Locate and identify every blood parasite.
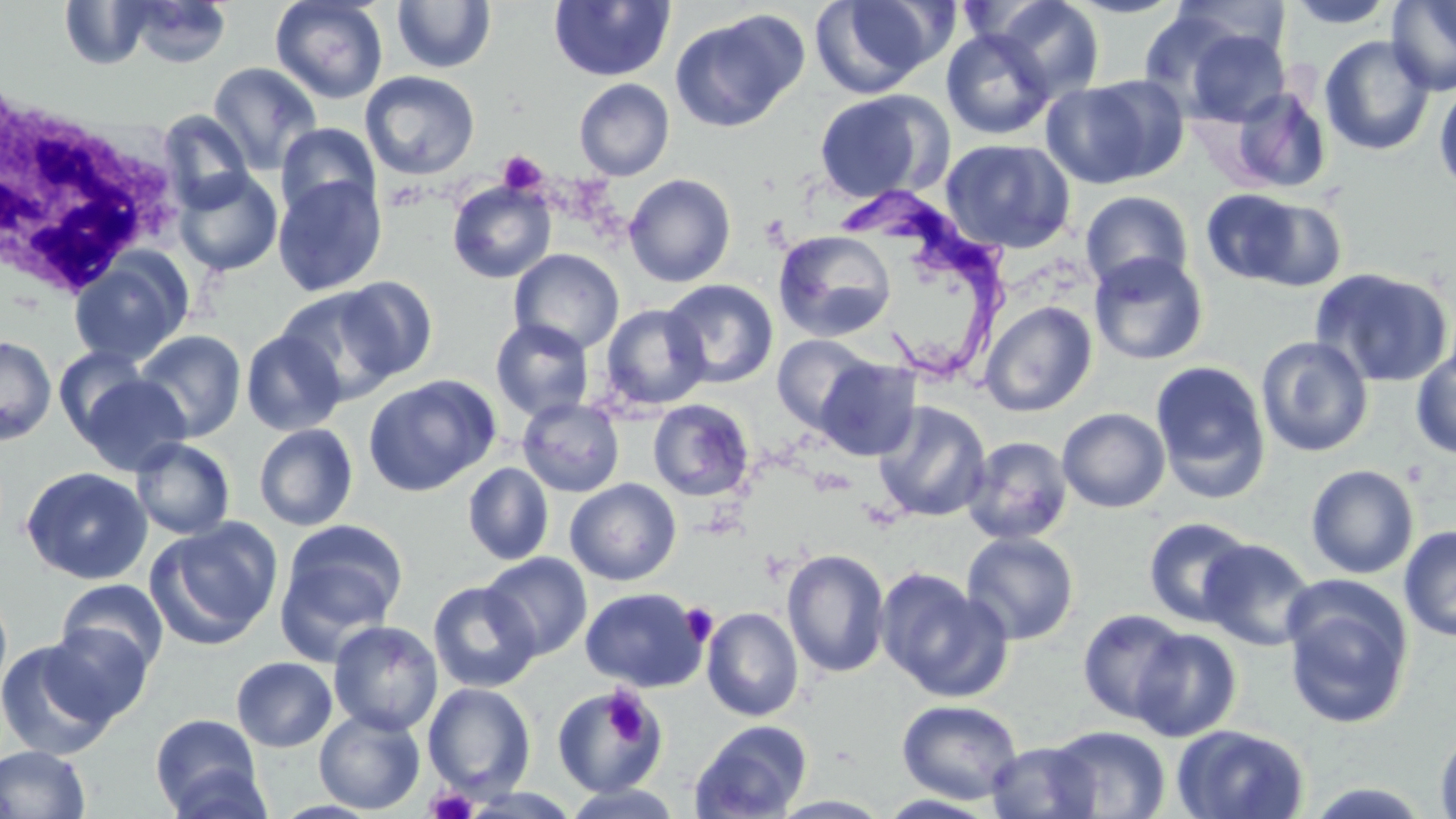

Approximate bounding boxes as named x1/y1/x2/y2 corners in pixels.
Trypanosoma brucei: (x1=843, y1=188, x2=1015, y2=387).
No Plasmodium falciparum, Plasmodium ovale, Plasmodium malariae, Plasmodium vivax, or Babesia divergens observed.

slide-level diagnosis = Trypanosoma brucei
field of view = single
stain = May-Grünwald-Giemsa
white blood cell locations = approximate bounding boxes as named x1/y1/x2/y2 corners in pixels: (x1=1, y1=98, x2=186, y2=296)
modality = light microscopy
platelet locations = approximate bounding boxes as named x1/y1/x2/y2 corners in pixels: (x1=497, y1=150, x2=547, y2=196), (x1=678, y1=602, x2=719, y2=646), (x1=601, y1=689, x2=660, y2=747), (x1=425, y1=786, x2=479, y2=819)
image size = 1456×819 pixels
magnification = 1000x
preparation = thin blood film
uninfected red blood cell locations = approximate bounding boxes as named x1/y1/x2/y2 corners in pixels: (x1=270, y1=0, x2=389, y2=104), (x1=391, y1=0, x2=496, y2=74), (x1=810, y1=0, x2=946, y2=98), (x1=988, y1=0, x2=1105, y2=102), (x1=1065, y1=0, x2=1187, y2=19), (x1=1167, y1=0, x2=1292, y2=66), (x1=1284, y1=0, x2=1399, y2=28), (x1=1387, y1=0, x2=1456, y2=96), (x1=59, y1=1, x2=152, y2=69), (x1=548, y1=1, x2=675, y2=82), (x1=124, y1=2, x2=233, y2=68), (x1=1138, y1=7, x2=1255, y2=114), (x1=670, y1=10, x2=809, y2=133), (x1=941, y1=29, x2=1055, y2=140), (x1=1182, y1=29, x2=1291, y2=127), (x1=1319, y1=35, x2=1435, y2=156), (x1=207, y1=61, x2=323, y2=175), (x1=359, y1=71, x2=480, y2=180), (x1=1042, y1=77, x2=1176, y2=188), (x1=574, y1=78, x2=674, y2=181), (x1=1434, y1=80, x2=1456, y2=197), (x1=1229, y1=86, x2=1332, y2=194), (x1=812, y1=90, x2=948, y2=204), (x1=156, y1=110, x2=254, y2=212), (x1=275, y1=123, x2=380, y2=222), (x1=940, y1=138, x2=1076, y2=254), (x1=173, y1=168, x2=283, y2=276), (x1=624, y1=173, x2=736, y2=287), (x1=272, y1=175, x2=387, y2=296), (x1=447, y1=181, x2=556, y2=284), (x1=1201, y1=188, x2=1309, y2=286), (x1=1080, y1=190, x2=1194, y2=293), (x1=1240, y1=195, x2=1350, y2=293), (x1=773, y1=230, x2=898, y2=342), (x1=509, y1=249, x2=624, y2=355), (x1=68, y1=251, x2=193, y2=367), (x1=1088, y1=252, x2=1209, y2=366), (x1=1310, y1=267, x2=1454, y2=388), (x1=335, y1=276, x2=439, y2=382), (x1=662, y1=279, x2=778, y2=388), (x1=275, y1=286, x2=402, y2=404), (x1=979, y1=301, x2=1097, y2=417), (x1=599, y1=303, x2=712, y2=411), (x1=490, y1=318, x2=595, y2=422), (x1=240, y1=329, x2=347, y2=436), (x1=134, y1=330, x2=246, y2=441), (x1=771, y1=334, x2=878, y2=433), (x1=1256, y1=335, x2=1374, y2=457), (x1=0, y1=336, x2=56, y2=445), (x1=56, y1=346, x2=152, y2=444), (x1=1411, y1=351, x2=1456, y2=459), (x1=814, y1=358, x2=921, y2=461), (x1=1150, y1=360, x2=1271, y2=503), (x1=78, y1=374, x2=191, y2=475), (x1=363, y1=375, x2=500, y2=497), (x1=517, y1=398, x2=625, y2=497), (x1=647, y1=399, x2=754, y2=501), (x1=874, y1=401, x2=990, y2=521), (x1=1057, y1=408, x2=1170, y2=513), (x1=253, y1=423, x2=358, y2=531), (x1=962, y1=436, x2=1074, y2=546), (x1=131, y1=438, x2=235, y2=540), (x1=462, y1=462, x2=554, y2=566), (x1=1305, y1=464, x2=1420, y2=579), (x1=21, y1=466, x2=153, y2=584), (x1=565, y1=478, x2=682, y2=586), (x1=1143, y1=517, x2=1256, y2=627), (x1=147, y1=518, x2=283, y2=650), (x1=275, y1=520, x2=408, y2=658), (x1=1398, y1=524, x2=1456, y2=642), (x1=961, y1=531, x2=1079, y2=645), (x1=1199, y1=537, x2=1317, y2=651), (x1=781, y1=548, x2=890, y2=678), (x1=480, y1=552, x2=593, y2=661), (x1=876, y1=568, x2=1012, y2=704), (x1=56, y1=579, x2=168, y2=674), (x1=427, y1=580, x2=541, y2=692), (x1=1281, y1=581, x2=1415, y2=730), (x1=0, y1=584, x2=13, y2=703), (x1=580, y1=587, x2=707, y2=692), (x1=701, y1=607, x2=804, y2=722), (x1=1077, y1=608, x2=1190, y2=724), (x1=328, y1=620, x2=443, y2=736), (x1=43, y1=622, x2=154, y2=725), (x1=1131, y1=627, x2=1242, y2=742), (x1=0, y1=638, x2=118, y2=761), (x1=232, y1=657, x2=337, y2=752), (x1=422, y1=682, x2=536, y2=799), (x1=553, y1=686, x2=667, y2=797), (x1=896, y1=699, x2=1024, y2=804), (x1=314, y1=709, x2=425, y2=814), (x1=151, y1=713, x2=266, y2=816), (x1=690, y1=719, x2=812, y2=818), (x1=1045, y1=725, x2=1170, y2=818), (x1=1171, y1=725, x2=1310, y2=818), (x1=1435, y1=728, x2=1456, y2=819), (x1=986, y1=740, x2=1102, y2=818), (x1=0, y1=744, x2=92, y2=819), (x1=160, y1=765, x2=275, y2=819), (x1=1302, y1=781, x2=1436, y2=819), (x1=560, y1=784, x2=684, y2=818)